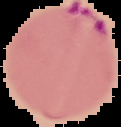
Malaria status: parasitized. The area outside the segmented cell region is set to black. Image is 121×127 pixels. From a thin blood smear.